Evaluate for Plasmodium parasites.
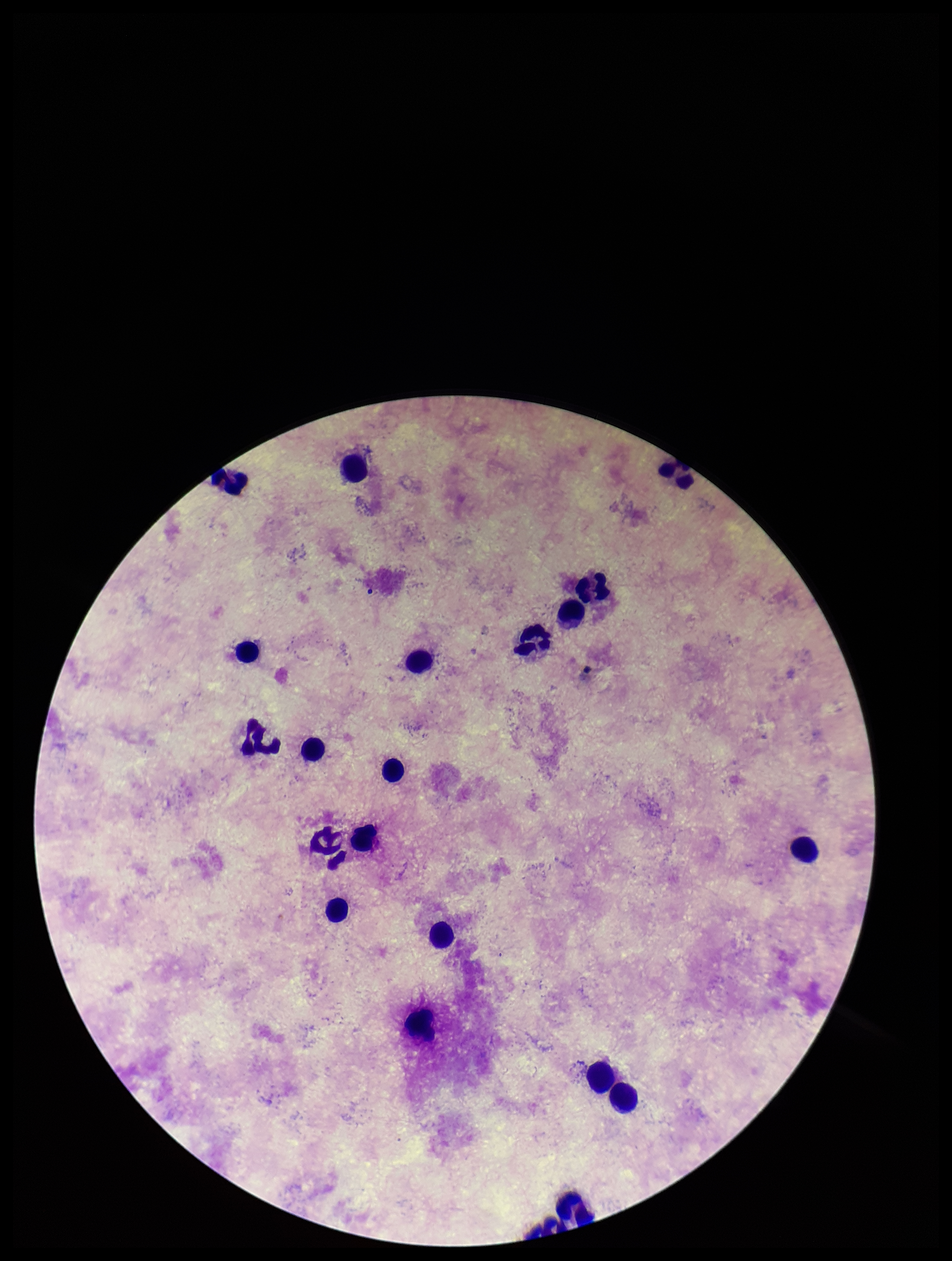

None identified.

Parasite count: 0. Giemsa stain. Preparation: thick. Smartphone photograph taken through the eyepiece of a microscope. Single field of view. Leukocyte count: 21. Patient malaria status: negative. Image is 952×1261 pixels.